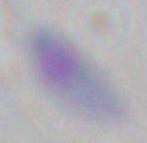
Toxoplasma gondii is shown. Photomicrograph. 1000x magnification.